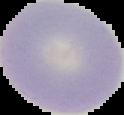

Summary:
  - Image type: segmented cell region with the area outside set to black
  - Image size: 124×115 pixels
  - Preparation: thin blood smear
  - Malaria status: uninfected